Describe the morphology of the erythrocytes.
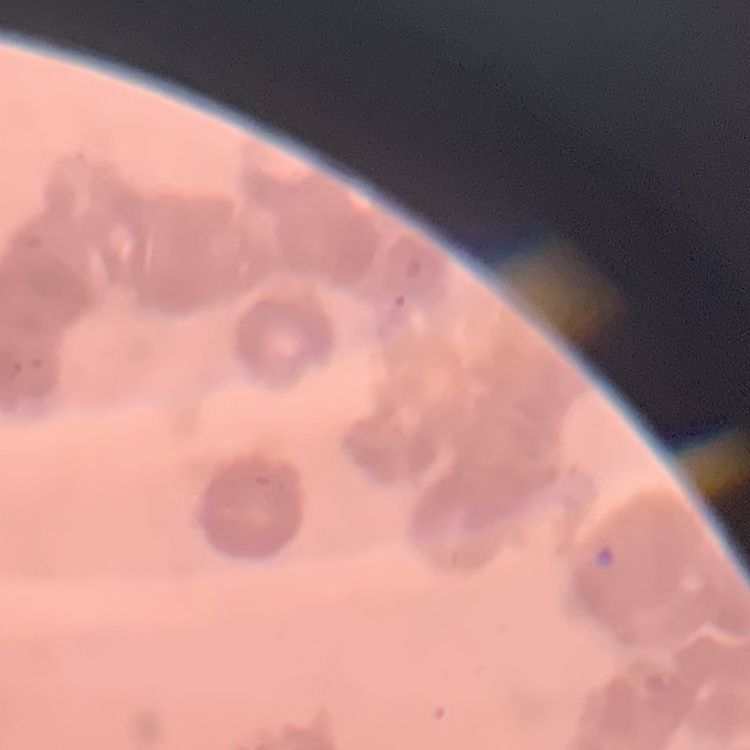

They show rouleaux formation.

Square crop of a larger photomicrograph. Thin peripheral smear. Stained with either Field's or Giemsa.